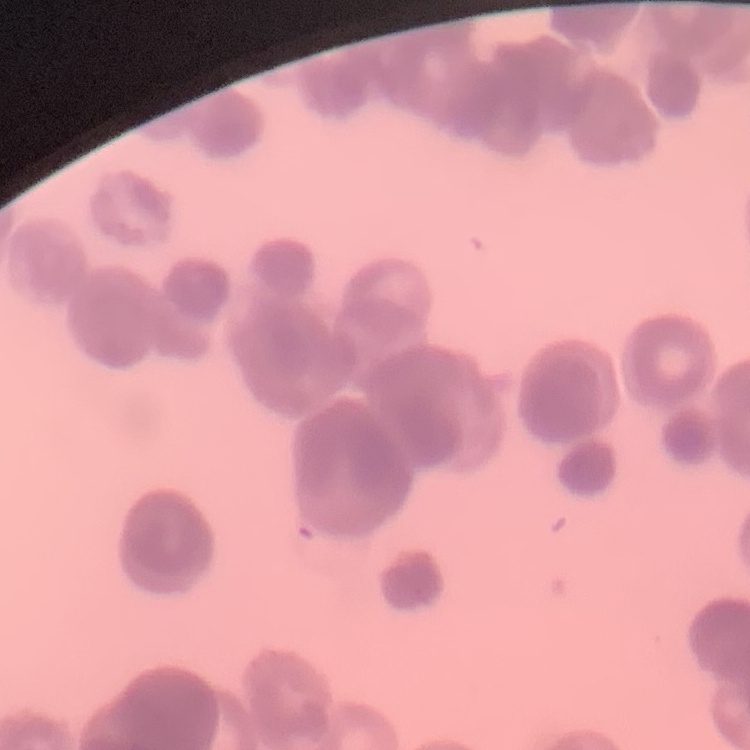

Summary:
  - Red blood cell morphology: rouleaux formation
  - Image type: square crop of a larger photomicrograph
  - Preparation: thin blood smear
  - Stain: Field's or Giemsa